State which parasite is depicted.
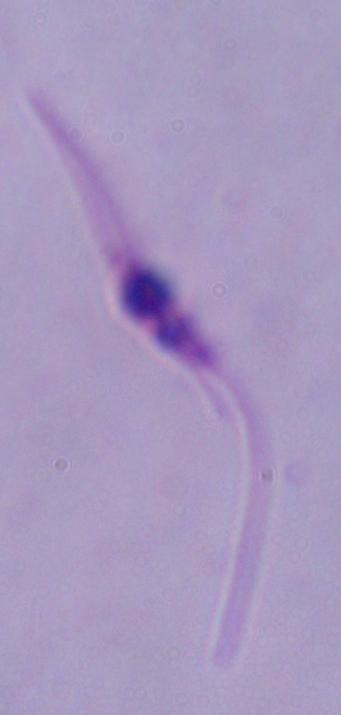
This is Leishmania.

Summary:
  - Modality: micrograph
  - Magnification: 1000x